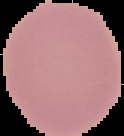

{
  "image_type": "segmented cell region on a black background",
  "malaria_status": "uninfected",
  "image_size": "124×136 pixels",
  "preparation": "thin blood film"
}